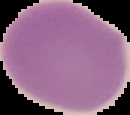 Cell region segmented out of the field of view; the surrounding area is masked to black. Result: no Plasmodium parasites detected. Image is 130×115 pixels. From a thin blood smear.